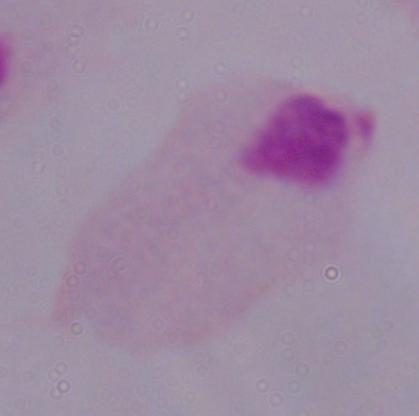

Summary:
  - Identification: trichomonad
  - Modality: micrograph
  - Magnification: 1000x